Name the parasite shown.
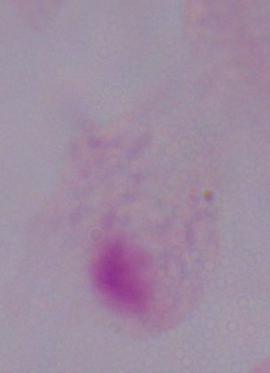

A trichomonad.

Summary:
  - Modality: photomicrograph
  - Magnification: 1000x